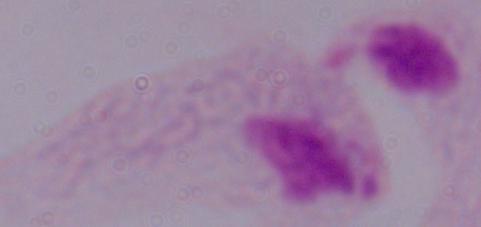

Summary:
  - Identification: trichomonad
  - Magnification: 1000x
  - Modality: photomicrograph